State which parasite is depicted.
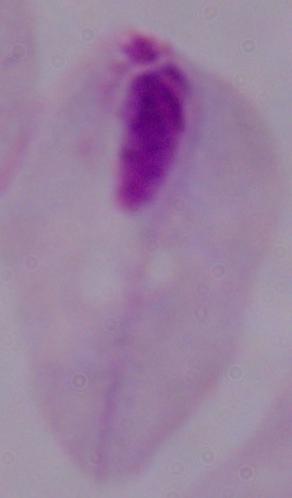

This is a trichomonad.

modality = micrograph
magnification = 1000x